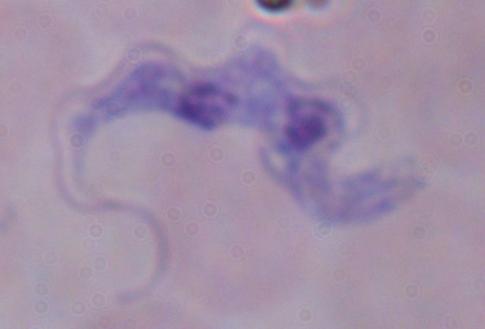

A trypanosome is shown. Micrograph. 1000x magnification.